Describe the morphology of the erythrocytes.
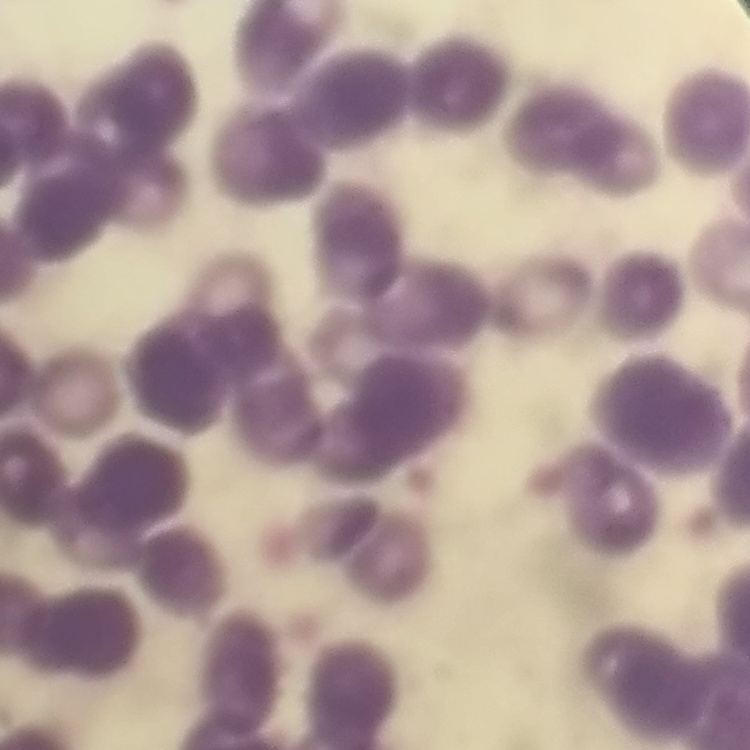

Rouleaux formation.

Summary:
  - Image type: one tile cut from a larger photomicrograph
  - Preparation: thin peripheral smear
  - Stain: Field's or Giemsa